Assess this cell for malaria.
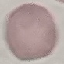
Uninfected.

Summary:
  - Preparation: thin smear
  - Image type: automatically extracted cell patch, resized to 64 × 64 pixels
  - Stain: Giemsa
  - Capture: smartphone through the microscope eyepiece